Assess the morphology of the red blood cells.
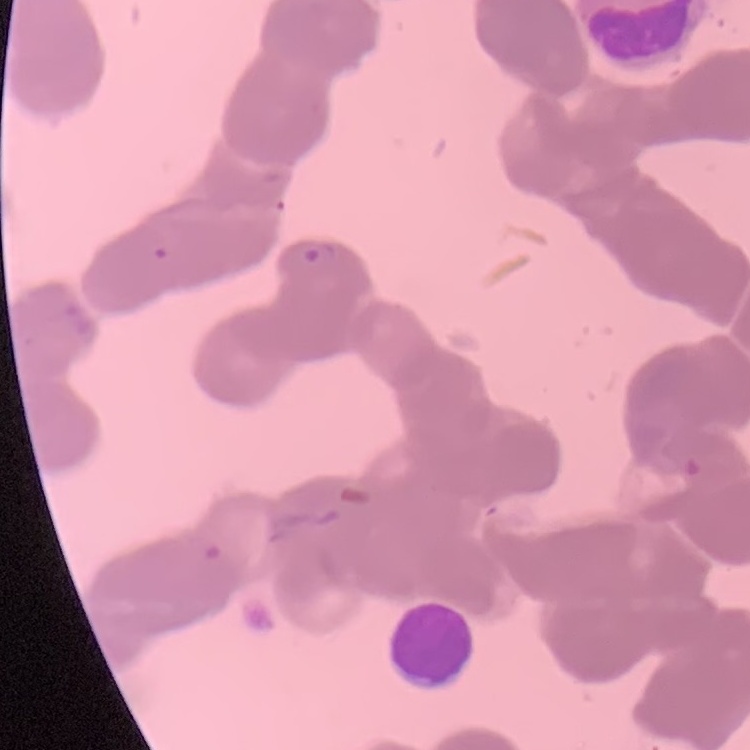
They show rouleaux formation.

One tile cut from a larger photomicrograph. Thin peripheral smear. Field's or Giemsa stain.